Report the malaria status of this cell.
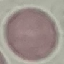
Uninfected.

Summary:
  - Capture: smartphone camera at the microscope eyepiece
  - Preparation: thin blood smear
  - Image type: automatically extracted cell patch, resized to 64 × 64 pixels
  - Stain: Giemsa